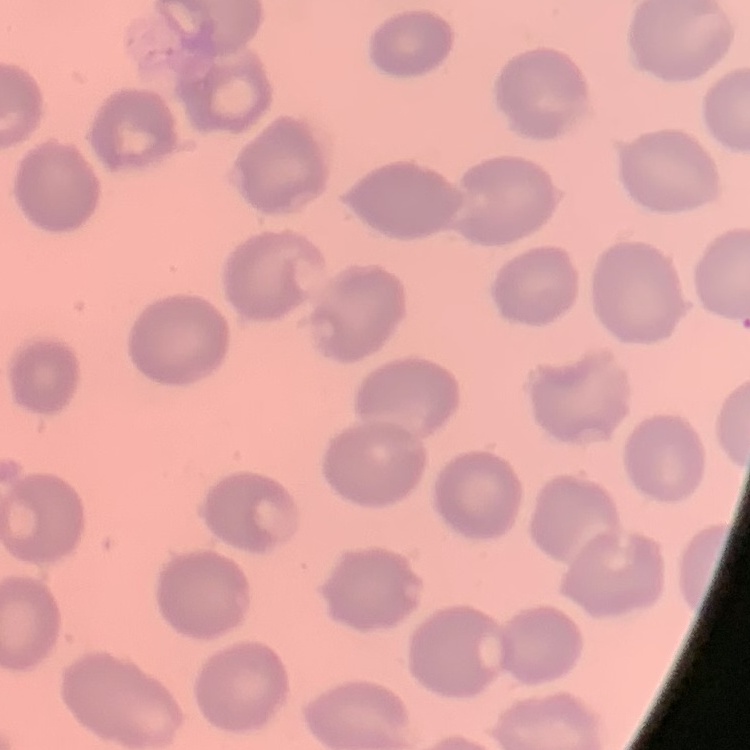 The red blood cells show no rouleaux formation. Square crop of a larger photomicrograph. Stained with either Field's or Giemsa. Thin peripheral smear.